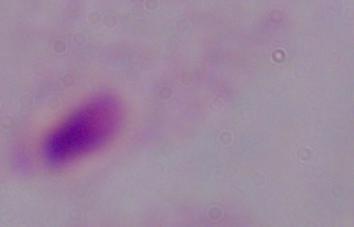

Summary:
  - Magnification: 1000x
  - Identification: trichomonad
  - Modality: micrograph